Point out each malaria parasite.
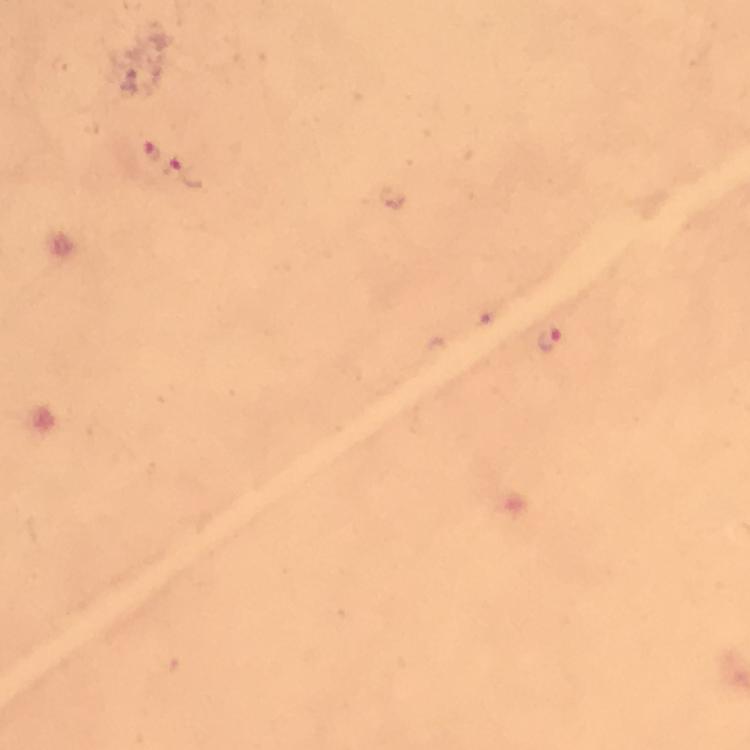
Approximate centers as [x, y] in pixels.
Malaria parasites: [149, 152], [187, 179], [487, 315], [550, 341].

stain: Giemsa
image_size: 750×750 pixels
immersion_oil: applied
preparation: thick smear
cropped_from: a single field of view
magnification: 100x
capture: smartphone camera through the microscope
context: from a diagnostic examination for malaria